Report the malaria status of this cell.
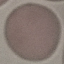

It is uninfected.

Thin blood smear. Giemsa-stained preparation. Cell patch, automatically extracted from a larger field of view and resized to 64 × 64 pixels. Photographed with a smartphone camera at the microscope eyepiece.